State which cell type is depicted.
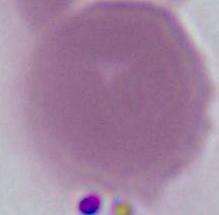
An erythrocyte.

Micrograph. 1000x magnification.